Locate every malaria parasite by life-cycle stage, and every leukocyte.
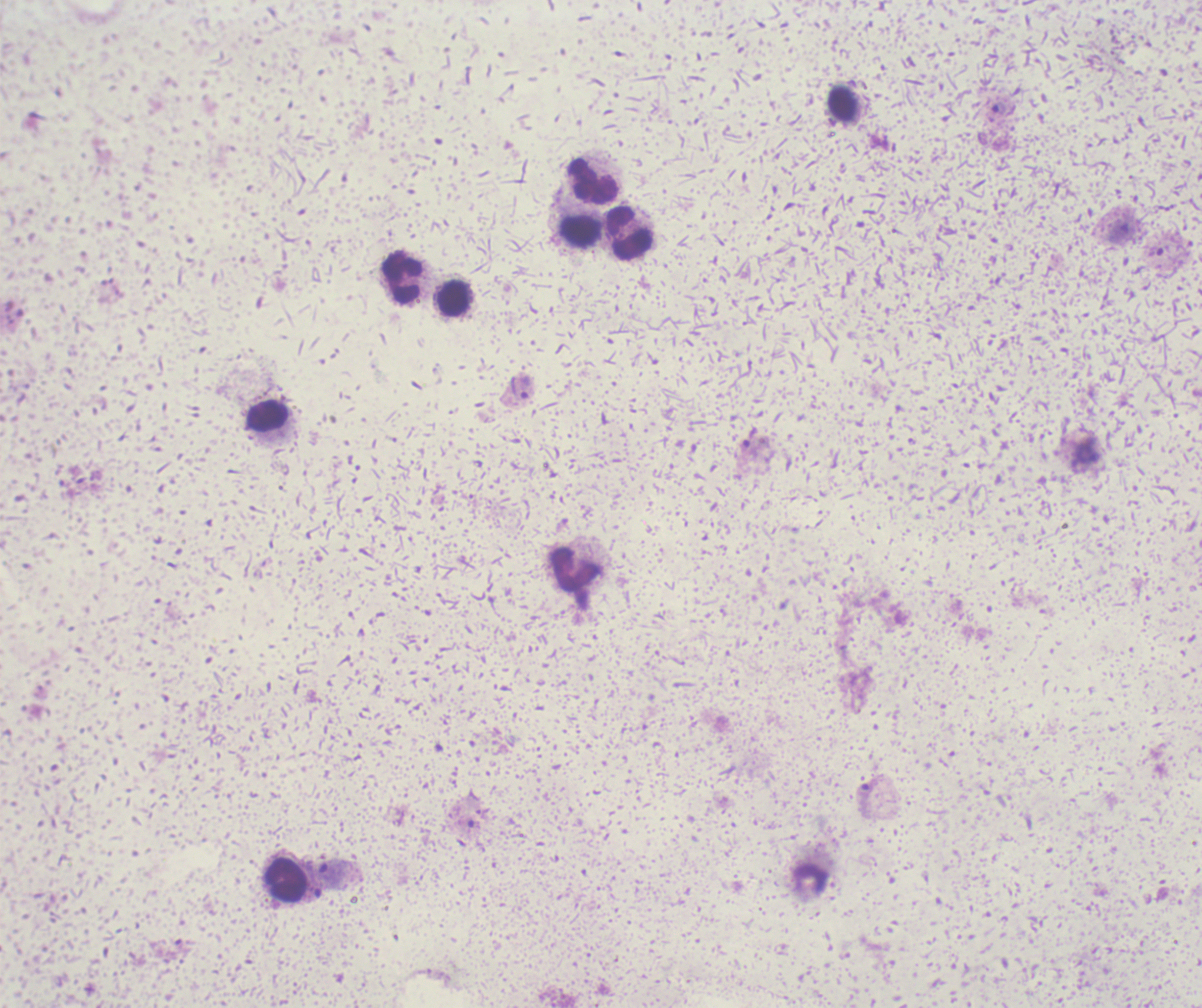

Approximate centers as [x, y] in pixels.
Trophozoites: [999, 108], [526, 387], [332, 871].
No schizont or gametocyte forms observed.
Leukocytes: [842, 102], [593, 181], [580, 231], [629, 232], [402, 278], [454, 298], [268, 417], [576, 569], [286, 880].

Previously used in an actual diagnosis. Thick smear of blood. 100x magnification. Image is 1202×1008 pixels. Single field of view. Romanowsky-stained preparation. Background quality: poor.